Assess this cell for malaria.
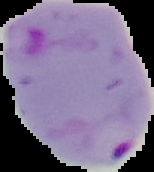
It is parasitized.

From a thin blood film. The area outside the segmented cell region is set to black. Image is 154×172 pixels.